State which parasite is depicted.
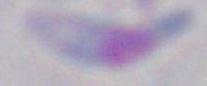
This is Toxoplasma gondii.

Summary:
  - Modality: photomicrograph
  - Magnification: 1000x